Evaluate for malaria.
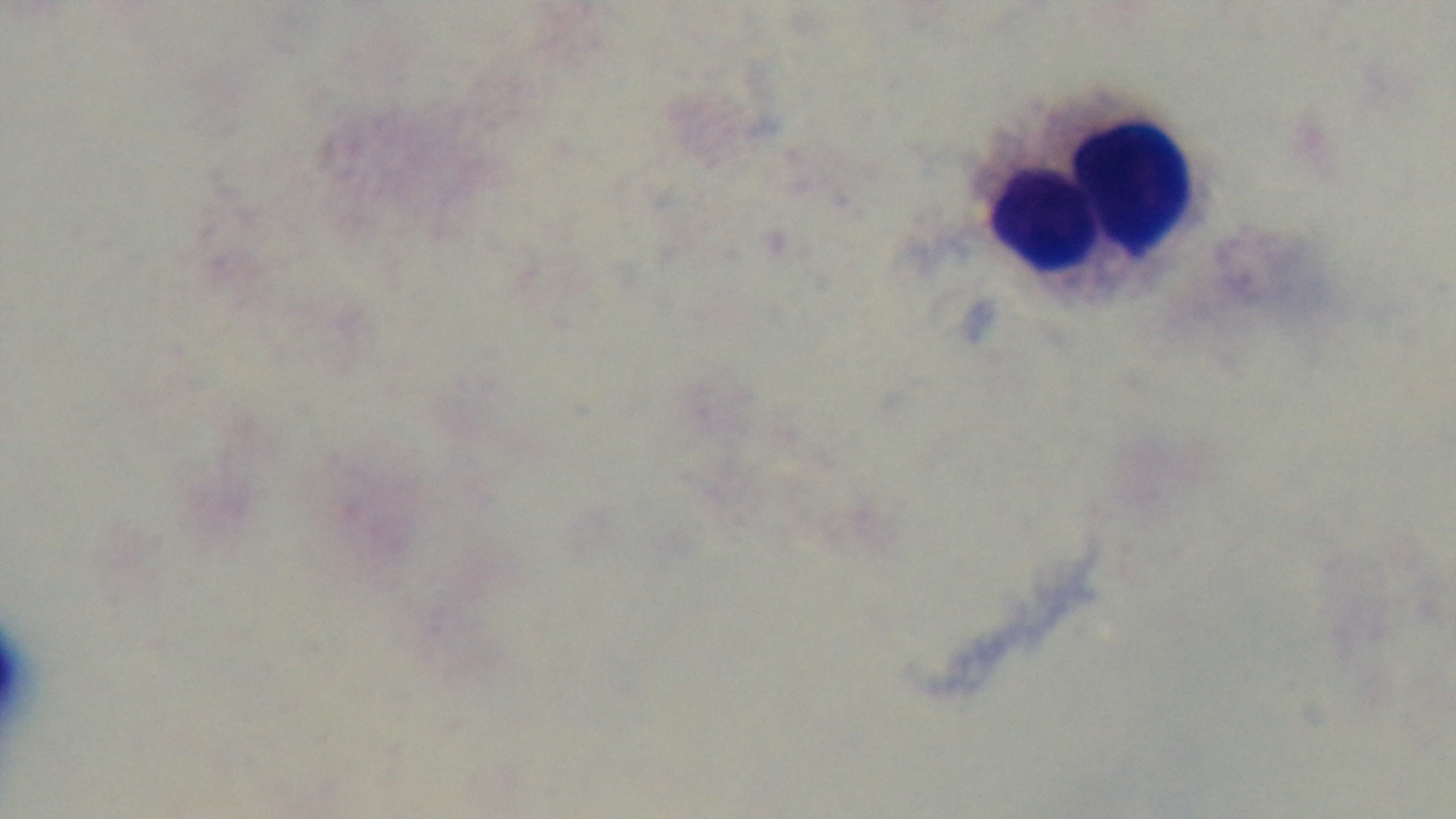

Uninfected.

preparation: thick blood film
stain: Giemsa
modality: light microscopy
capture: mounted 4K digital camera
field_of_view: one from the slide
objective: 100x oil immersion